Identify the parasite.
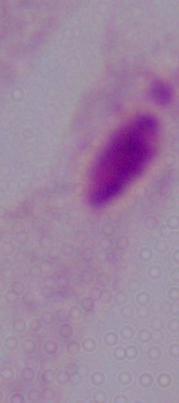

This is a trichomonad.

1000x magnification. Micrograph.